Evaluate for malaria.
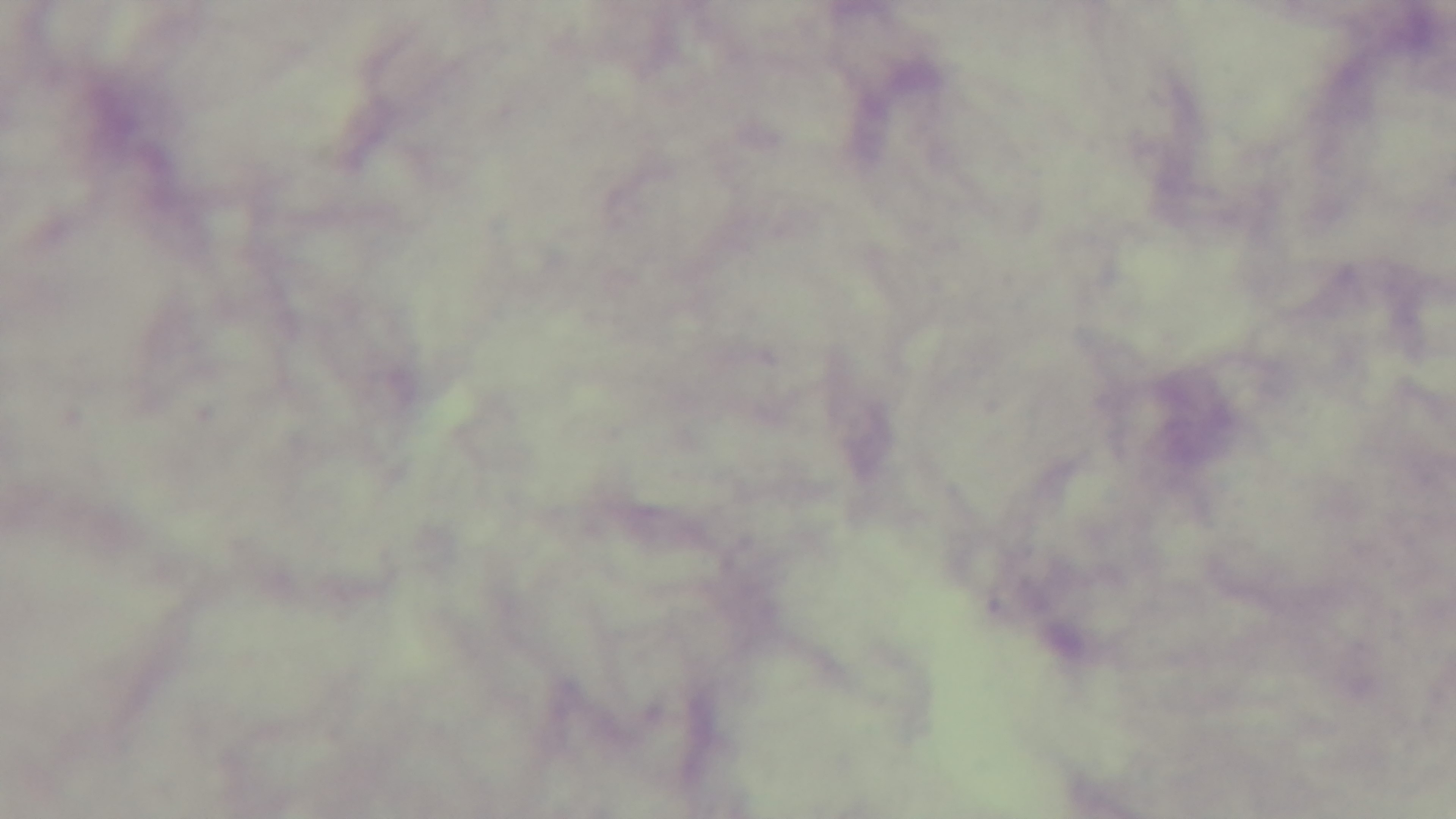

It is uninfected.

Mounted 4K digital camera. One field from the slide. Preparation: thick blood film. Giemsa-stained. Light microscopy. 100x oil-immersion objective.